Name the parasite shown.
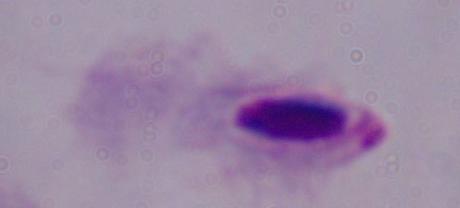
A trichomonad.

Summary:
  - Modality: photomicrograph
  - Magnification: 1000x